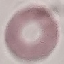
Malaria status: uninfected. Giemsa-stained preparation. Acquired by smartphone through the microscope eyepiece. Automatically extracted cell patch, resized to 64 × 64 pixels. Thin blood film.